Find the red blood cells that are infected with Plasmodium falciparum, and any of indeterminate infection status.
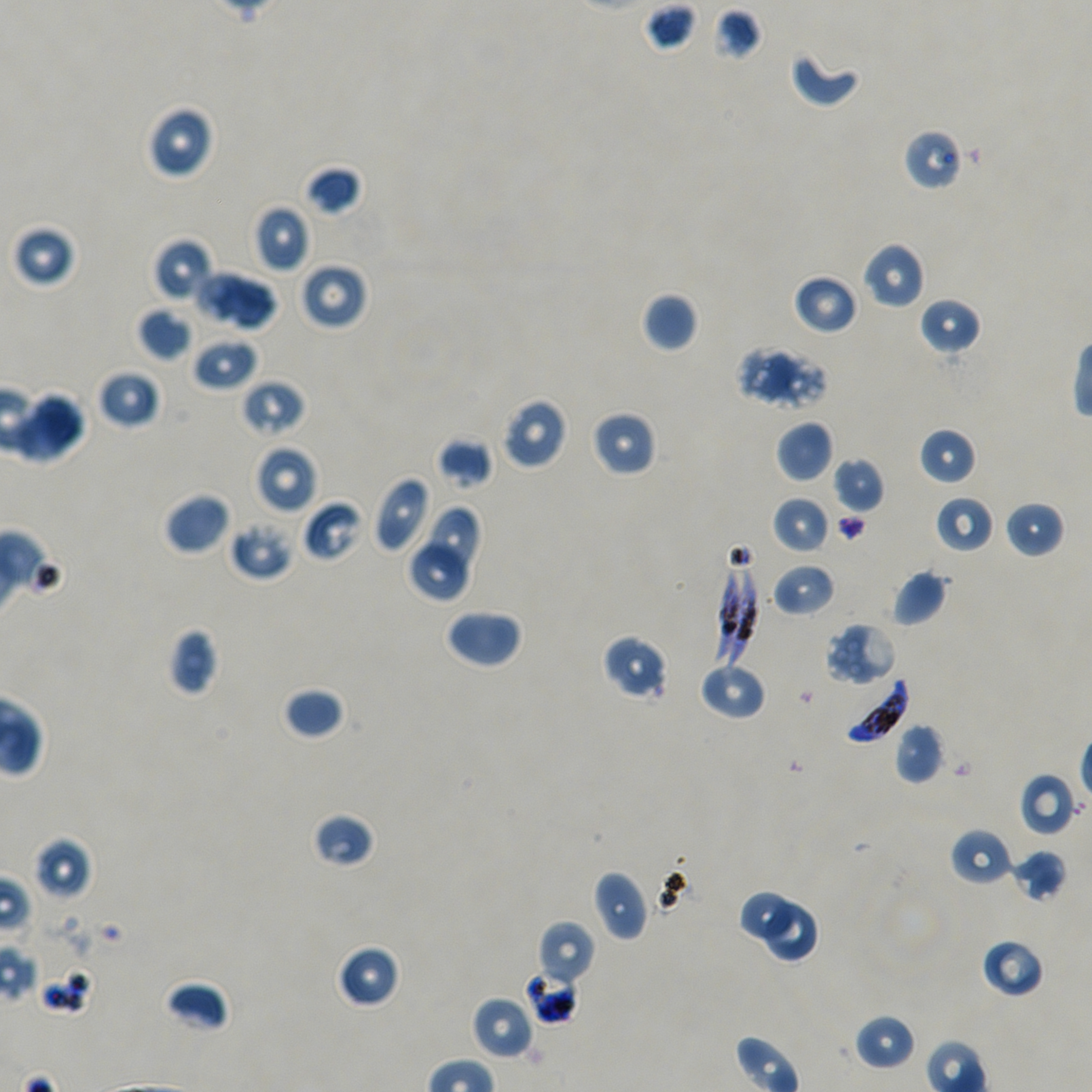

Approximate bounding boxes as {x1, y1, x2, y2} in pixels. Not every red blood cell is marked.
Infected red blood cells: {733, 544, 759, 665}, {713, 546, 744, 666}, {841, 678, 909, 745}.
Red blood cells of indeterminate infection status: {37, 966, 94, 1015}, {525, 968, 579, 1025}.

Locations of uninfected red blood cells: {640, 2, 700, 54}, {712, 7, 763, 61}, {789, 48, 862, 108}, {145, 105, 214, 179}, {902, 128, 963, 192}, {304, 164, 364, 217}, {254, 204, 310, 272}, {14, 225, 76, 287}, {153, 238, 215, 304}, {862, 242, 926, 310}, {299, 261, 369, 331}, {194, 270, 256, 327}, {793, 273, 858, 335}, {227, 278, 280, 334}, {642, 292, 698, 353}, {919, 297, 981, 355}, {137, 307, 194, 362}, {192, 338, 257, 391}, {736, 344, 798, 405}, {770, 346, 829, 416}, {97, 369, 160, 429}, {242, 380, 307, 437}, {32, 392, 85, 454}, {500, 397, 569, 470}, {591, 410, 657, 477}, {14, 413, 70, 463}, {776, 420, 834, 483}, {918, 426, 977, 486}, {437, 437, 494, 490}, {253, 445, 318, 515}, {833, 456, 886, 514}, {371, 475, 432, 553}, {164, 493, 230, 555}, {771, 495, 830, 555}, {935, 495, 994, 553}, {302, 500, 365, 563}, {1004, 501, 1066, 559}, {428, 505, 483, 570}, {228, 518, 296, 581}, {407, 545, 472, 602}, {771, 562, 835, 617}, {890, 569, 947, 627}, {445, 608, 524, 670}, {824, 622, 898, 687}, {168, 627, 219, 695}, {601, 634, 669, 702}, {699, 663, 766, 720}, {283, 687, 346, 740}, {894, 722, 945, 784}, {1019, 772, 1076, 836}, {311, 812, 377, 869}, {951, 828, 1013, 886}, {34, 837, 92, 900}, {1008, 848, 1067, 903}, {593, 869, 649, 941}, {742, 892, 790, 939}, {765, 903, 817, 960}, {535, 920, 596, 989}, {981, 938, 1045, 998}, {336, 943, 401, 1009}, {163, 981, 230, 1032}, {471, 996, 534, 1059}, {854, 1014, 917, 1071}. Blood group of the donor: A+/O+. Image is 1092×1092 pixels. Thin blood smear. 100x objective under oil immersion, numerical aperture 1.45. Static in-vitro culture of Plasmodium falciparum strain NF54. Giemsa stain. One field from this slide.